Assess this cell for malaria.
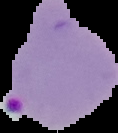
Parasitized.

{
  "image_size": "118×133 pixels",
  "image_type": "segmented cell region with the area outside set to black",
  "preparation": "thin blood film"
}